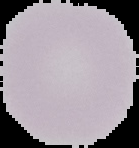

{
  "image_size": "139×148 pixels",
  "malaria_status": "uninfected",
  "preparation": "thin blood film",
  "image_type": "segmented cell region on a black background"
}